Assess the morphology of the erythrocytes.
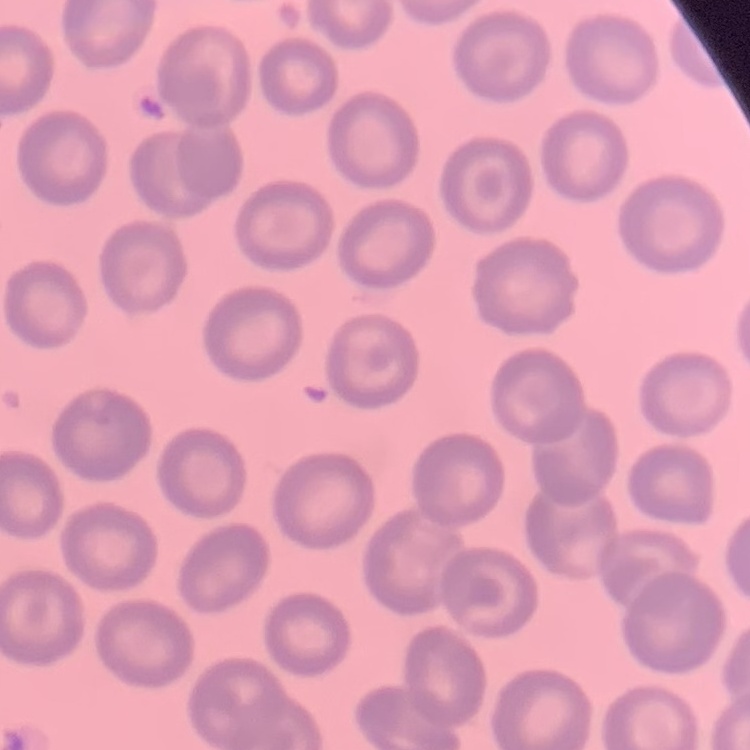
They show no rouleaux formation.

{
  "preparation": "thin blood film",
  "image_type": "one tile cut from a larger photomicrograph",
  "stain": "Field's or Giemsa"
}